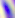

Captured at 400x magnification. Micrograph. Toxoplasma gondii is seen.